Locate every blood parasite and identify its species.
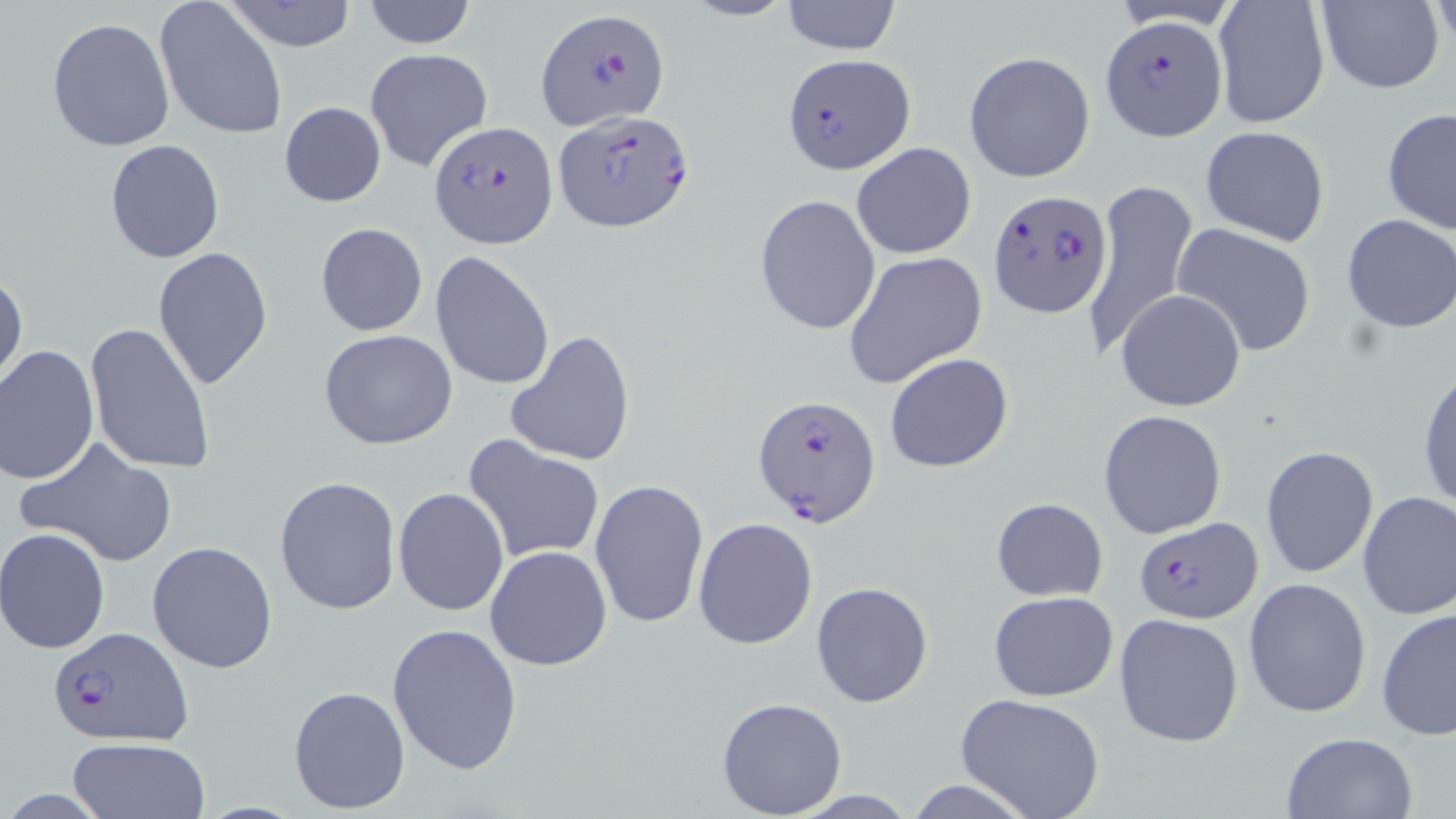

Approximate bounding boxes as named x1/y1/x2/y2 corners in pixels.
Plasmodium falciparum-infected red blood cells: (x1=535, y1=7, x2=670, y2=131), (x1=1100, y1=12, x2=1227, y2=144), (x1=783, y1=53, x2=916, y2=177), (x1=553, y1=109, x2=696, y2=231), (x1=430, y1=120, x2=555, y2=245), (x1=989, y1=190, x2=1111, y2=319), (x1=753, y1=394, x2=881, y2=529), (x1=1133, y1=517, x2=1263, y2=624), (x1=48, y1=625, x2=192, y2=747).
No Plasmodium ovale, Plasmodium malariae, Plasmodium vivax, Babesia divergens, or Trypanosoma brucei observed.

Summary:
  - Uninfected red blood cell locations: (x1=223, y1=0, x2=357, y2=51), (x1=361, y1=0, x2=477, y2=49), (x1=678, y1=0, x2=797, y2=23), (x1=1315, y1=0, x2=1443, y2=95), (x1=155, y1=1, x2=288, y2=140), (x1=779, y1=1, x2=902, y2=55), (x1=1107, y1=1, x2=1248, y2=32), (x1=1212, y1=1, x2=1331, y2=129), (x1=47, y1=17, x2=175, y2=152), (x1=364, y1=48, x2=493, y2=171), (x1=963, y1=51, x2=1095, y2=184), (x1=280, y1=102, x2=386, y2=206), (x1=1380, y1=107, x2=1456, y2=234), (x1=1200, y1=125, x2=1330, y2=247), (x1=104, y1=139, x2=226, y2=264), (x1=850, y1=142, x2=977, y2=260), (x1=1082, y1=178, x2=1198, y2=360), (x1=754, y1=194, x2=880, y2=335), (x1=1340, y1=214, x2=1456, y2=333), (x1=1172, y1=221, x2=1316, y2=356), (x1=315, y1=223, x2=428, y2=336), (x1=152, y1=246, x2=274, y2=390), (x1=842, y1=250, x2=987, y2=390), (x1=431, y1=251, x2=555, y2=390), (x1=0, y1=267, x2=26, y2=390), (x1=1115, y1=288, x2=1246, y2=412), (x1=85, y1=322, x2=217, y2=476), (x1=318, y1=329, x2=459, y2=449), (x1=505, y1=329, x2=637, y2=468), (x1=0, y1=343, x2=99, y2=486), (x1=884, y1=352, x2=1014, y2=473), (x1=1418, y1=366, x2=1456, y2=513), (x1=1098, y1=409, x2=1227, y2=541), (x1=463, y1=436, x2=605, y2=565), (x1=18, y1=438, x2=179, y2=568), (x1=1261, y1=446, x2=1378, y2=578), (x1=273, y1=475, x2=401, y2=615), (x1=589, y1=477, x2=709, y2=627), (x1=393, y1=488, x2=508, y2=616), (x1=1357, y1=491, x2=1456, y2=621), (x1=991, y1=497, x2=1108, y2=601), (x1=692, y1=518, x2=818, y2=649), (x1=1, y1=528, x2=110, y2=653), (x1=147, y1=540, x2=278, y2=672), (x1=485, y1=545, x2=612, y2=670), (x1=1243, y1=577, x2=1371, y2=719), (x1=811, y1=581, x2=933, y2=707), (x1=988, y1=591, x2=1119, y2=702), (x1=1377, y1=605, x2=1456, y2=744), (x1=1114, y1=613, x2=1244, y2=747), (x1=386, y1=621, x2=523, y2=775), (x1=288, y1=684, x2=411, y2=814), (x1=955, y1=694, x2=1105, y2=818), (x1=717, y1=697, x2=848, y2=818), (x1=1279, y1=730, x2=1419, y2=819), (x1=67, y1=736, x2=212, y2=819), (x1=905, y1=779, x2=1035, y2=818), (x1=787, y1=788, x2=920, y2=818)
  - Slide-level diagnosis: Plasmodium falciparum
  - Modality: light microscopy
  - Magnification: 1000x
  - Stain: May-Grünwald-Giemsa
  - Preparation: thin blood smear
  - Field of view: one of a larger specimen
  - Image size: 1456×819 pixels